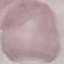
Summary:
  - Malaria status: uninfected
  - Preparation: thin blood smear
  - Capture: smartphone through the microscope eyepiece
  - Image type: automatically extracted cell patch, resized to 64 × 64 pixels
  - Stain: Giemsa